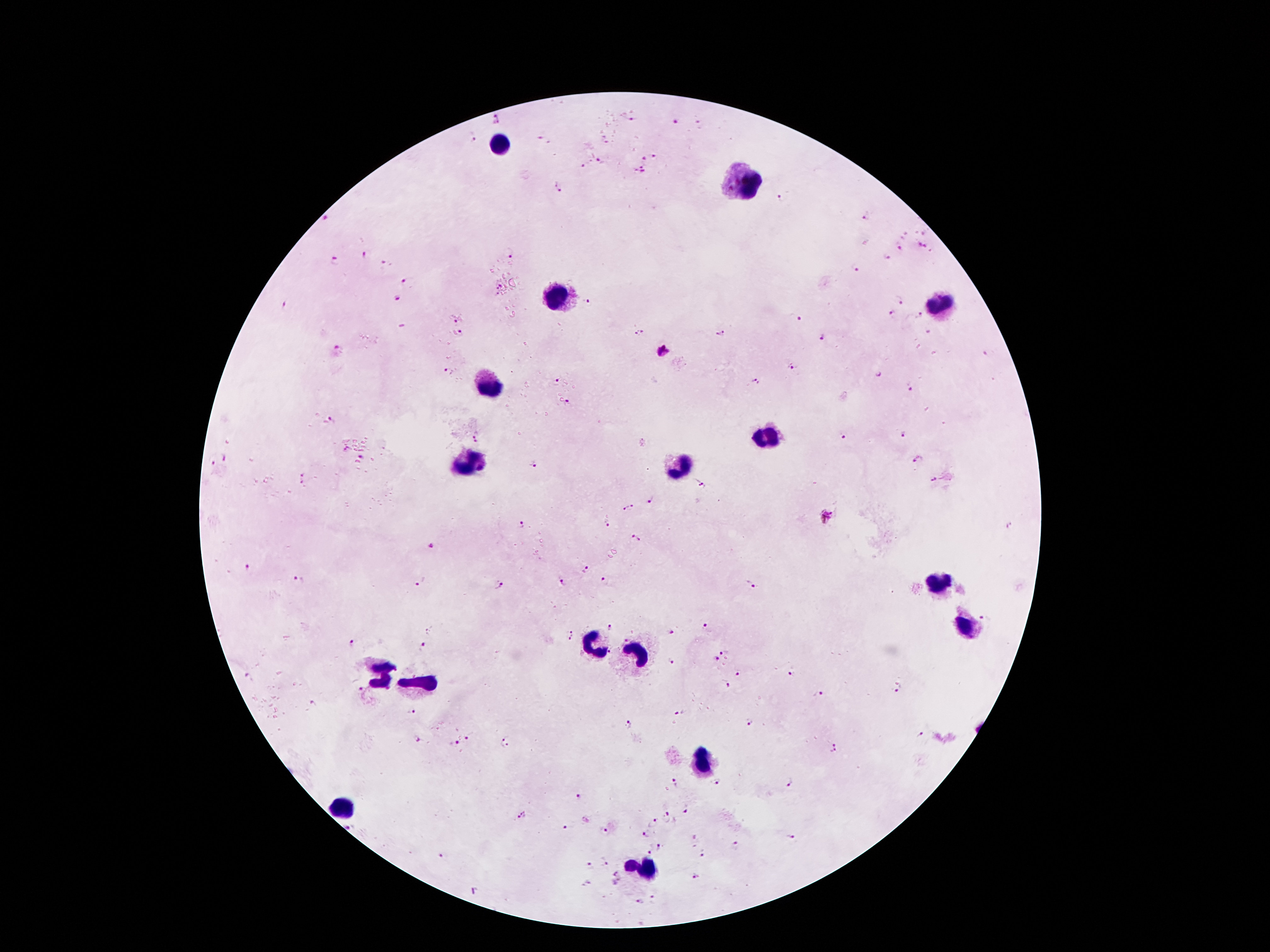

coordinate format = approximate centers as {x, y} in pixels
malaria parasite locations = {499, 117}, {632, 119}, {676, 122}, {542, 137}, {474, 138}, {606, 142}, {654, 156}, {644, 158}, {599, 162}, {581, 167}, {639, 171}, {559, 189}, {781, 198}, {865, 215}, {329, 217}, {923, 232}, {923, 245}, {897, 247}, {366, 253}, {510, 254}, {886, 257}, {335, 262}, {385, 263}, {855, 269}, {407, 281}, {499, 287}, {496, 296}, {899, 297}, {398, 299}, {587, 299}, {285, 304}, {891, 314}, {918, 316}, {799, 319}, {453, 322}, {640, 331}, {459, 333}, {719, 333}, {824, 336}, {339, 347}, {663, 352}, {794, 366}, {447, 372}, {877, 373}, {557, 381}, {757, 382}, {909, 388}, {566, 402}, {330, 421}, {904, 435}, {843, 437}, {477, 439}, {345, 450}, {225, 454}, {361, 458}, {918, 459}, {213, 461}, {534, 462}, {302, 475}, {930, 480}, {702, 484}, {649, 501}, {628, 509}, {827, 517}, {521, 524}, {607, 525}, {1008, 527}, {635, 537}, {429, 548}, {246, 567}, {586, 569}, {298, 580}, {563, 581}, {420, 582}, {604, 582}, {501, 583}, {750, 583}, {983, 617}, {610, 626}, {705, 627}, {671, 632}, {568, 636}, {352, 643}, {421, 645}, {723, 650}, {608, 653}, {717, 659}, {671, 660}, {790, 673}, {738, 674}, {248, 676}, {727, 684}, {897, 689}, {359, 691}, {389, 692}, {818, 692}, {313, 704}, {415, 709}, {677, 714}, {748, 721}, {629, 724}, {920, 733}, {467, 738}, {416, 739}, {506, 742}, {453, 744}, {834, 749}, {715, 782}, {675, 783}, {788, 783}, {578, 796}, {686, 811}, {521, 817}, {667, 817}, {651, 824}, {350, 826}, {565, 828}, {604, 833}, {643, 833}, {694, 837}, {792, 837}, {657, 845}, {734, 845}, {650, 849}, {703, 853}, {443, 855}, {605, 863}, {587, 864}, {614, 873}, {695, 875}, {588, 883}, {472, 891}, {654, 898}, {639, 901}
leukocyte locations = {502, 142}, {745, 183}, {556, 294}, {942, 303}, {486, 385}, {772, 433}, {468, 467}, {681, 467}, {936, 583}, {963, 623}, {590, 639}, {636, 653}, {377, 671}, {422, 680}, {697, 762}, {343, 810}, {640, 871}
stain = Giemsa
image size = 1270×952 pixels
patient malaria status = infected with Plasmodium falciparum
preparation = thick blood smear
magnification = 100x
field of view = single
capture = smartphone camera through the microscope eyepiece